Name the cell type shown.
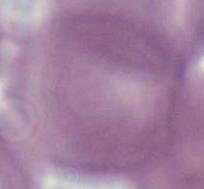
This is an erythrocyte.

modality = micrograph
magnification = 1000x